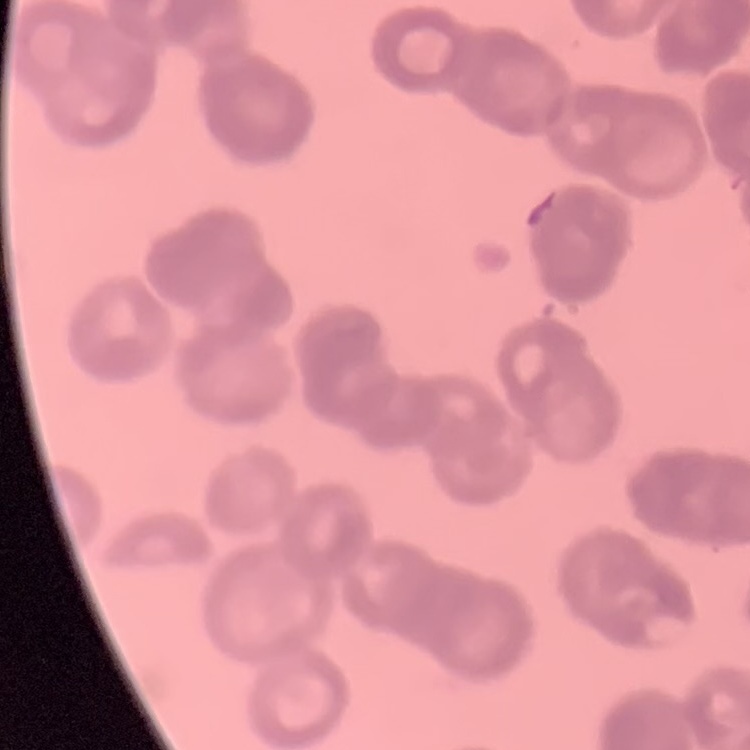 The erythrocytes exhibit rouleaux formation. Square crop of a larger photomicrograph. Thin blood smear. Stained with either Field's or Giemsa.